Classify this cell by malaria status.
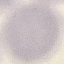

Uninfected.

capture = smartphone through the microscope eyepiece
preparation = thin smear
stain = Giemsa
image type = cell patch, automatically extracted from a larger field of view and resized to 64 × 64 pixels